Locate every Plasmodium parasite.
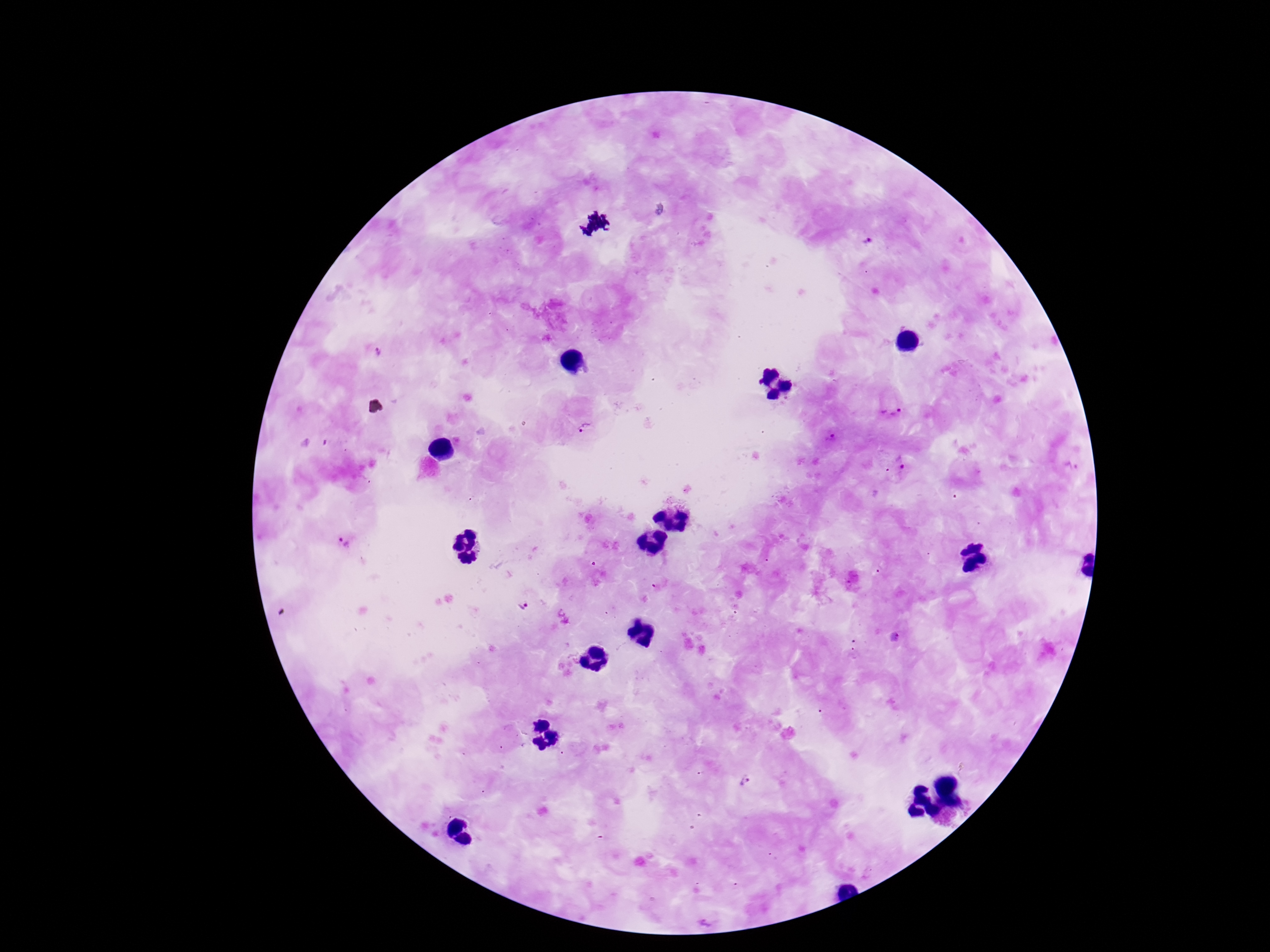
Approximate object centers, in pixels from the top-left corner.
Plasmodium parasites: (x=867, y=246), (x=379, y=351), (x=893, y=413), (x=585, y=428), (x=832, y=438), (x=897, y=464), (x=343, y=543), (x=524, y=605), (x=747, y=780).

stain = Giemsa
image size = 1270×952 pixels
patient malaria status = infected
capture = smartphone camera through the microscope eyepiece
magnification = 100x
preparation = thick peripheral-blood smear
field of view = one from this slide